Give the preparation type.
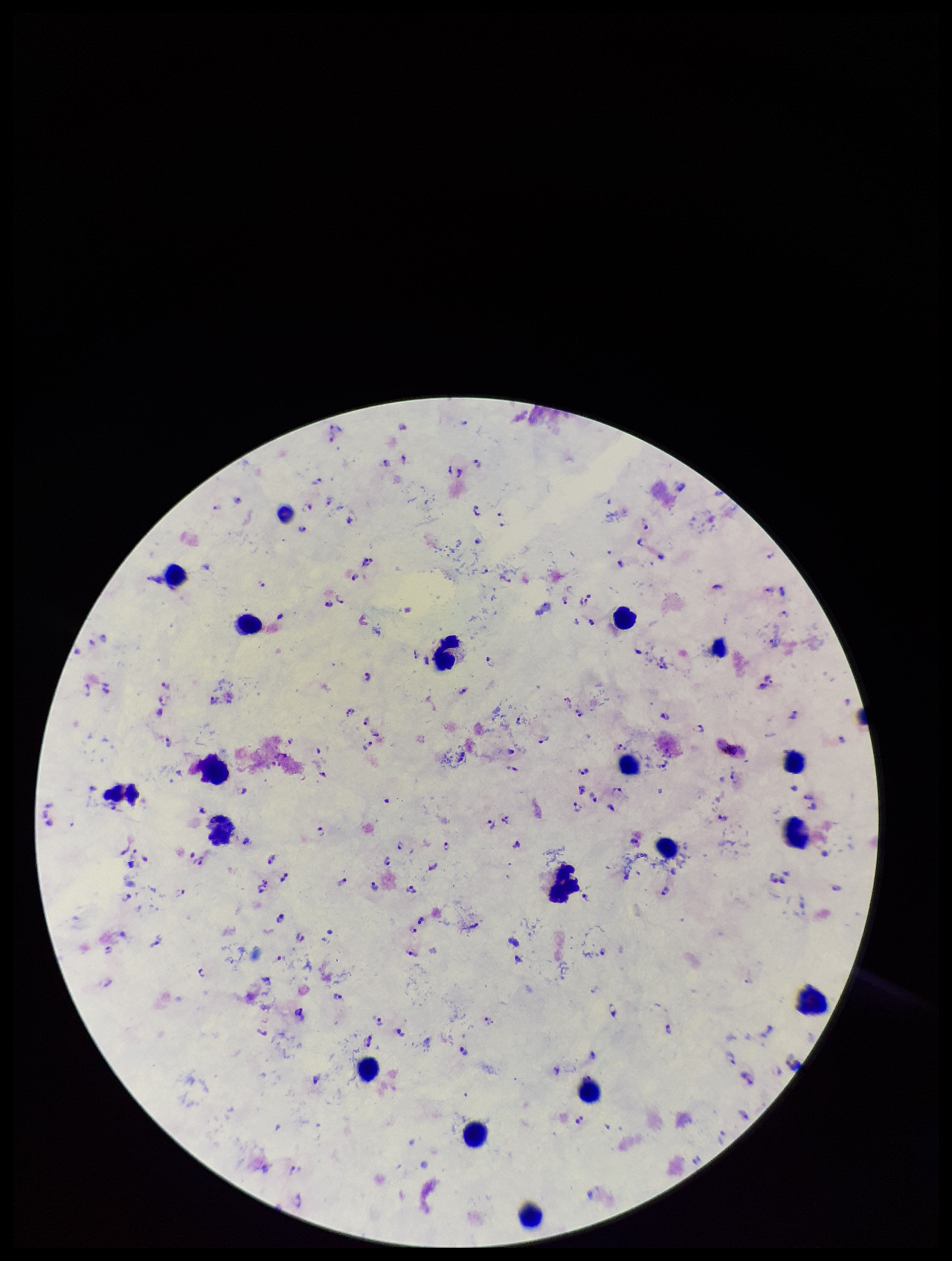
A thick smear.

Giemsa stain. Species reported for this patient: Plasmodium falciparum. Plasmodium parasites: identified. Leukocyte count: 19. Smartphone photograph taken through the eyepiece of a microscope. Parasite count: 125. One field from this slide. Patient malaria status: positive. Image is 952×1261 pixels.